Name the parasite shown.
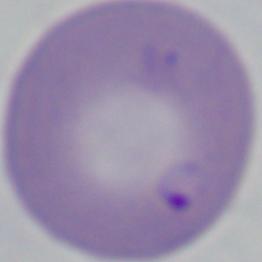
Babesia.

{
  "magnification": "1000x",
  "modality": "micrograph"
}